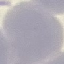
result = no malaria parasites seen
preparation = thin blood smear
stain = Giemsa
image type = automatically extracted cell patch, resized to 64 × 64 pixels
capture = smartphone camera at the microscope eyepiece